Locate every Plasmodium ovale-infected red blood cell.
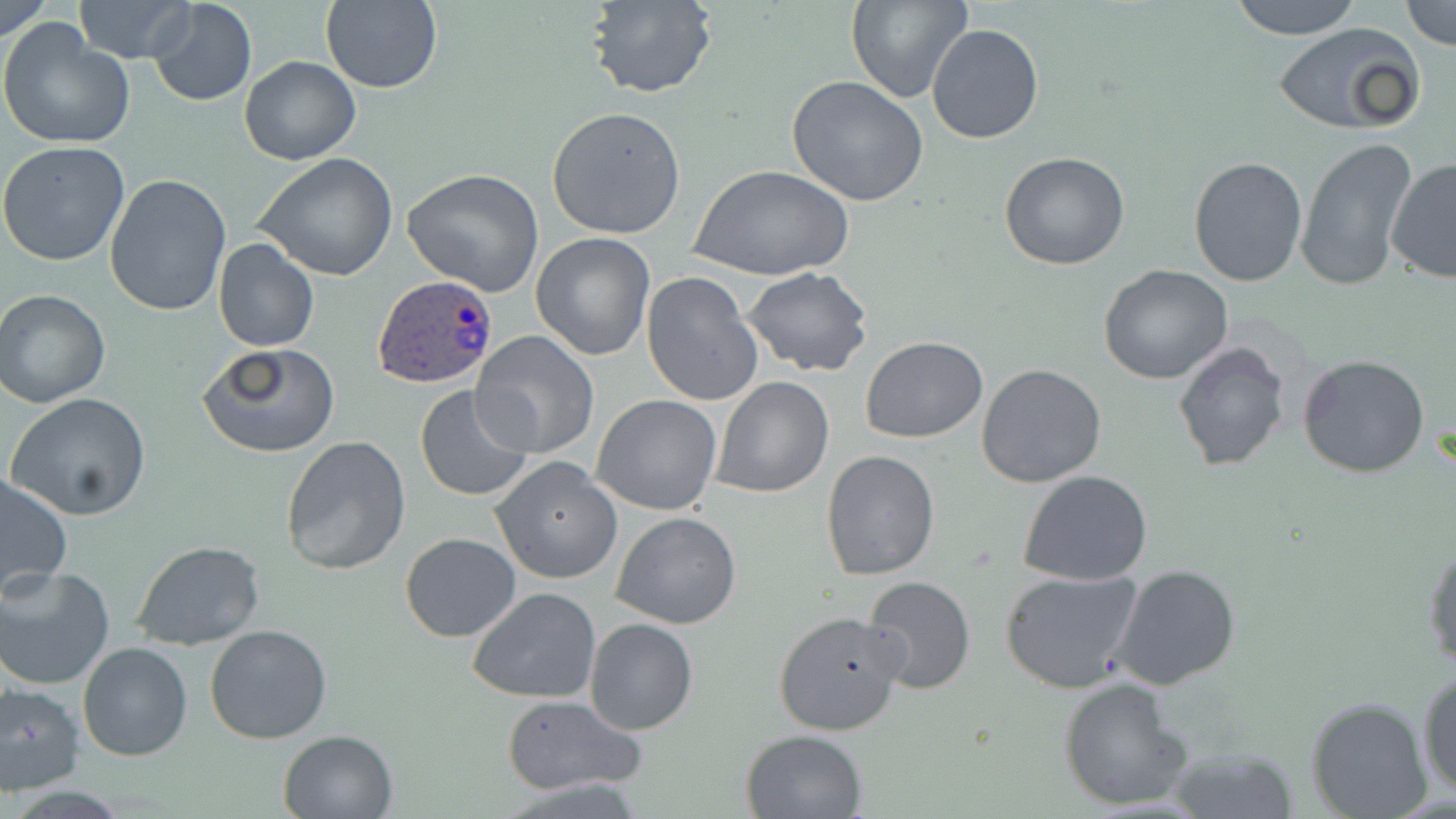

Approximate bounding boxes as (x1, y1, x2, y2) in pixels.
Plasmodium ovale-infected red blood cells: (375, 274, 497, 387).

Summary:
  - Uninfected red blood cell locations: (0, 0, 51, 46), (73, 0, 193, 63), (148, 0, 256, 107), (585, 0, 717, 99), (846, 0, 972, 105), (1230, 0, 1364, 38), (319, 1, 442, 92), (1400, 2, 1456, 49), (0, 20, 134, 149), (1272, 20, 1427, 136), (927, 23, 1044, 144), (240, 56, 361, 165), (786, 76, 930, 207), (547, 106, 687, 240), (1295, 137, 1420, 294), (0, 141, 130, 266), (999, 152, 1131, 271), (254, 154, 400, 282), (1188, 156, 1307, 286), (1385, 158, 1456, 285), (693, 164, 851, 282), (401, 168, 547, 297), (104, 174, 232, 317), (529, 232, 656, 360), (213, 239, 319, 352), (1099, 265, 1236, 385), (743, 268, 873, 379), (641, 272, 764, 408), (0, 288, 114, 408), (472, 332, 599, 460), (860, 337, 988, 442), (1173, 340, 1291, 472), (197, 343, 341, 459), (1298, 353, 1431, 478), (976, 363, 1107, 488), (711, 377, 834, 498), (412, 383, 535, 504), (6, 393, 152, 520), (592, 395, 722, 515), (280, 435, 412, 577), (821, 448, 941, 580), (490, 457, 623, 585), (1018, 471, 1153, 587), (0, 472, 74, 598), (611, 511, 742, 629), (400, 531, 521, 642), (1423, 537, 1456, 672), (133, 540, 266, 651), (1110, 563, 1242, 690), (0, 565, 115, 689), (999, 567, 1144, 692), (863, 575, 975, 693), (467, 587, 601, 702), (773, 609, 908, 737), (584, 618, 699, 735), (204, 624, 333, 743), (78, 642, 194, 762), (1416, 665, 1456, 801), (1058, 677, 1194, 812), (0, 682, 85, 794), (500, 695, 646, 798), (1303, 696, 1434, 819), (741, 728, 868, 818), (277, 729, 400, 818), (1166, 745, 1300, 818)
  - Slide-level diagnosis: Plasmodium ovale
  - Magnification: 1000x
  - Image size: 1456×819 pixels
  - Preparation: thin blood smear
  - Modality: optical microscopy
  - Field of view: single
  - Stain: May-Grünwald-Giemsa